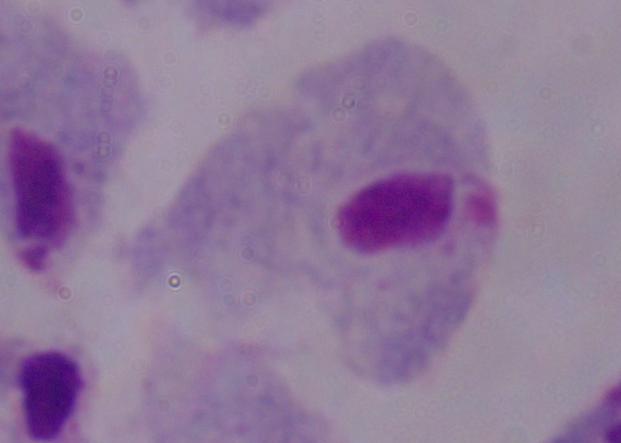

magnification = 1000x
identification = trichomonad
modality = micrograph